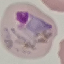

Summary:
  - Malaria status: uninfected
  - Preparation: thin smear
  - Stain: Giemsa
  - Capture: smartphone camera at the microscope eyepiece
  - Image type: cell patch, automatically extracted from a larger field of view and resized to 64 × 64 pixels